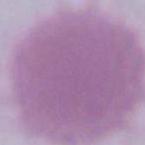

Summary:
  - Modality: micrograph
  - Identification: erythrocyte
  - Magnification: 1000x